Report the malaria status of this cell.
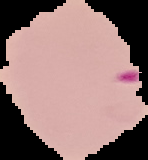

It is parasitized.

The area outside the segmented cell region is set to black. From a thin blood film. Image is 148×160 pixels.